Classify this cell by malaria status.
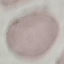
Uninfected.

image type = cell patch, automatically extracted from a larger field of view and resized to 64 × 64 pixels
capture = smartphone camera at the microscope eyepiece
stain = Giemsa
preparation = thin blood film